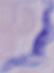
modality = photomicrograph
identification = trypanosome
magnification = 1000x